Locate every blood parasite and identify its species.
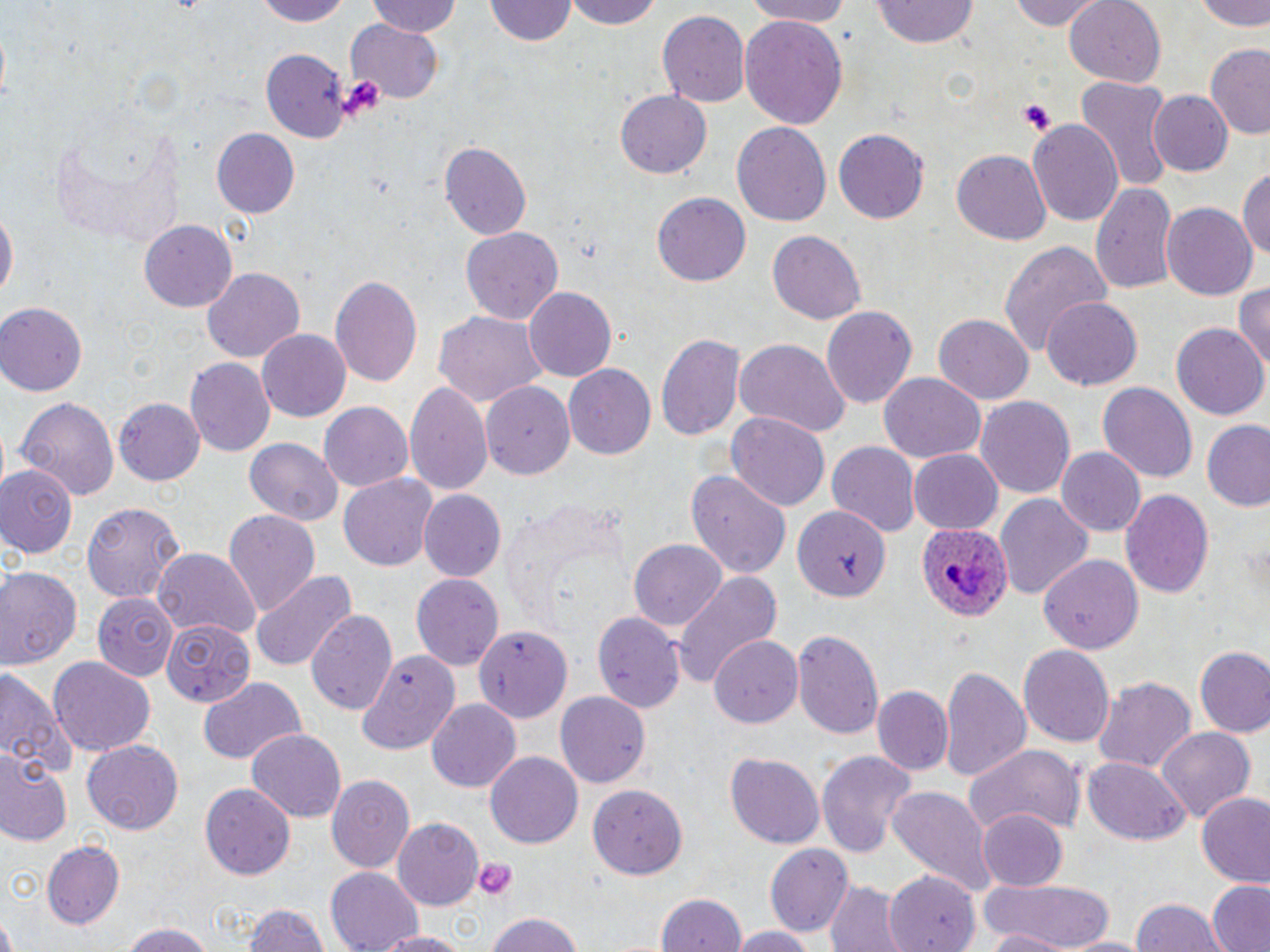
Approximate bounding boxes as [x1, y1, x2, y2] in pixels.
Plasmodium ovale-infected red blood cells: [914, 521, 1010, 622].
No Plasmodium falciparum, Plasmodium malariae, Plasmodium vivax, Babesia divergens, or Trypanosoma brucei observed.

Uninfected red blood cell locations: [251, 0, 352, 25], [362, 0, 465, 38], [486, 0, 577, 45], [560, 0, 669, 28], [739, 0, 862, 26], [1007, 0, 1108, 31], [1196, 0, 1270, 33], [1065, 1, 1166, 86], [872, 3, 983, 48], [658, 11, 750, 109], [738, 13, 848, 130], [346, 20, 443, 102], [1204, 45, 1270, 139], [258, 50, 351, 140], [1075, 79, 1172, 192], [615, 90, 712, 178], [1149, 90, 1231, 176], [1028, 119, 1124, 229], [732, 122, 832, 226], [212, 128, 301, 216], [834, 128, 930, 224], [439, 141, 532, 239], [952, 151, 1051, 244], [1238, 164, 1269, 268], [1090, 181, 1179, 292], [651, 192, 751, 287], [0, 204, 17, 307], [1164, 204, 1258, 301], [138, 221, 239, 311], [459, 226, 563, 326], [768, 229, 865, 323], [999, 239, 1112, 356], [201, 267, 306, 365], [330, 272, 424, 390], [1232, 280, 1270, 375], [524, 287, 618, 381], [1041, 298, 1143, 391], [0, 303, 88, 395], [821, 305, 916, 412], [433, 308, 544, 409], [933, 315, 1034, 406], [1171, 323, 1269, 421], [257, 329, 352, 420], [657, 332, 744, 441], [734, 337, 850, 439], [185, 359, 274, 458], [563, 364, 656, 460], [879, 373, 985, 464], [405, 381, 494, 500], [1097, 382, 1197, 482], [482, 383, 577, 481], [975, 394, 1075, 499], [16, 395, 120, 499], [114, 397, 206, 485], [320, 400, 414, 492], [726, 412, 830, 512], [1201, 422, 1270, 511], [246, 438, 343, 525], [827, 443, 920, 536], [1056, 447, 1147, 537], [910, 450, 1001, 533], [0, 466, 80, 556], [685, 469, 792, 580], [338, 474, 437, 571], [1120, 487, 1214, 599], [421, 491, 505, 580], [500, 493, 632, 634], [992, 493, 1093, 602], [79, 501, 186, 602], [793, 507, 891, 602], [223, 508, 320, 618], [629, 540, 726, 633], [154, 550, 258, 639], [1040, 553, 1144, 654], [0, 565, 83, 670], [250, 569, 355, 672], [670, 571, 784, 693], [410, 574, 503, 669], [91, 592, 179, 679], [306, 607, 396, 715], [593, 607, 687, 713], [163, 618, 256, 707], [469, 626, 568, 725], [792, 628, 883, 739], [709, 635, 802, 729], [1018, 645, 1115, 746], [1191, 645, 1270, 737], [355, 650, 461, 754], [47, 657, 156, 758], [938, 666, 1029, 783], [0, 667, 72, 781], [195, 675, 306, 767], [1091, 676, 1197, 776], [871, 686, 953, 775], [556, 690, 653, 788], [425, 699, 521, 791], [1155, 726, 1258, 822], [247, 730, 346, 819], [83, 739, 183, 836], [964, 745, 1084, 838], [815, 748, 917, 858], [726, 750, 825, 849], [486, 752, 582, 848], [0, 754, 70, 847], [1082, 757, 1189, 846], [325, 773, 416, 875], [198, 782, 295, 879], [589, 782, 690, 878], [887, 785, 997, 899], [1196, 792, 1270, 887], [976, 808, 1068, 890], [393, 818, 482, 907], [43, 840, 125, 929], [764, 842, 854, 936], [327, 867, 424, 951], [885, 868, 977, 951], [980, 877, 1118, 948], [825, 880, 903, 952], [1206, 882, 1270, 952], [654, 891, 750, 952], [1133, 895, 1228, 952], [240, 900, 330, 952], [483, 911, 586, 952], [0, 917, 21, 952], [120, 923, 219, 952], [728, 925, 818, 952], [977, 928, 1079, 952], [375, 930, 472, 952], [1058, 934, 1148, 952]. Platelet locations: [336, 75, 388, 121], [1017, 100, 1054, 135], [475, 858, 517, 900]. Slide-level diagnosis: Plasmodium ovale. Thin blood smear. Image is 1270×952 pixels. May-Grünwald-Giemsa-stained preparation. Single field of view. Light microscopy. Captured at 1000x magnification.